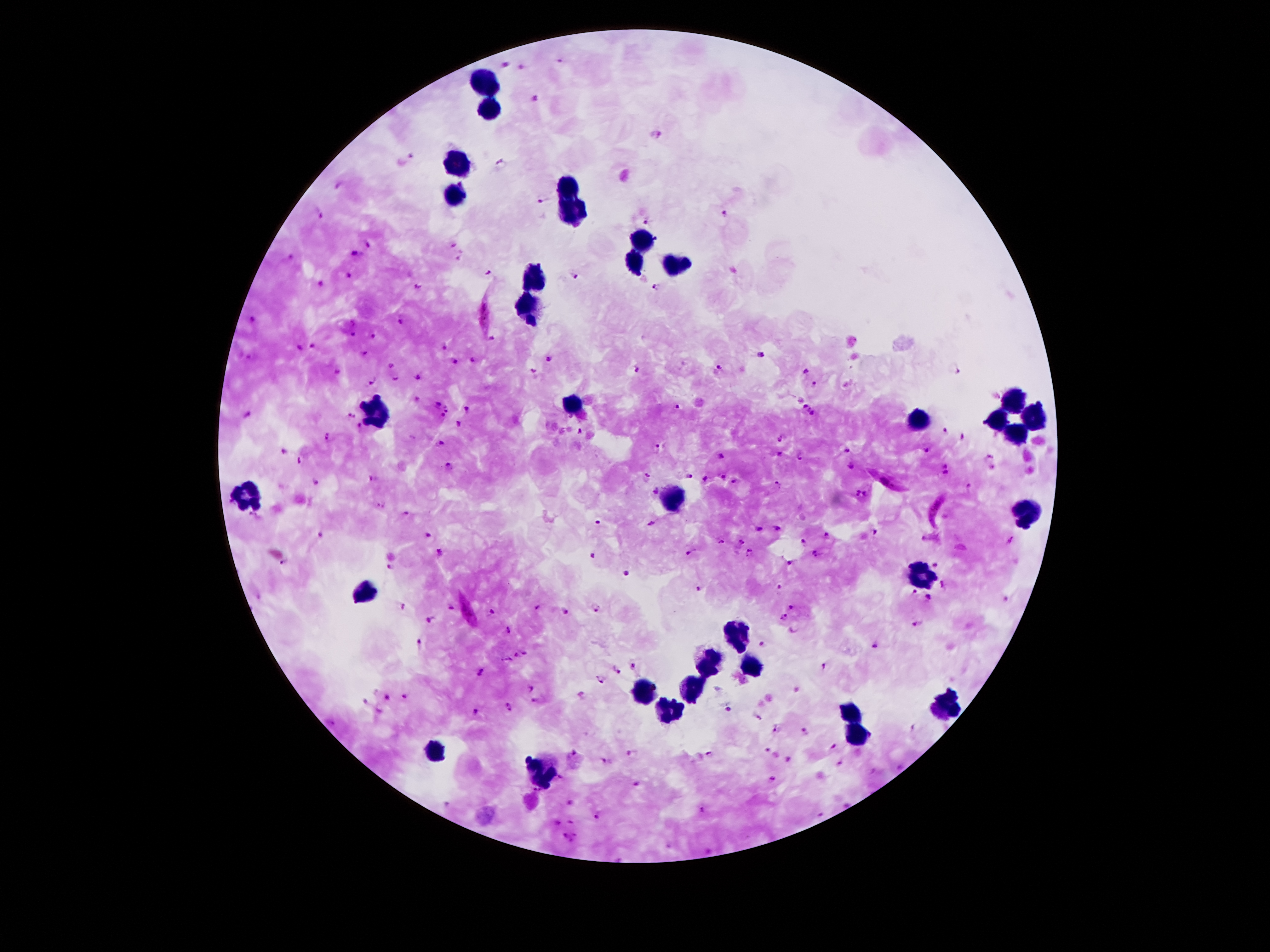 Patient malaria status: positive for Plasmodium falciparum. One field from this slide. 100x magnification. Image is 1270×952 pixels. Photographed through the microscope eyepiece with a smartphone camera. Giemsa stain. Thick peripheral-blood smear.